Locate every Plasmodium ovale-infected red blood cell.
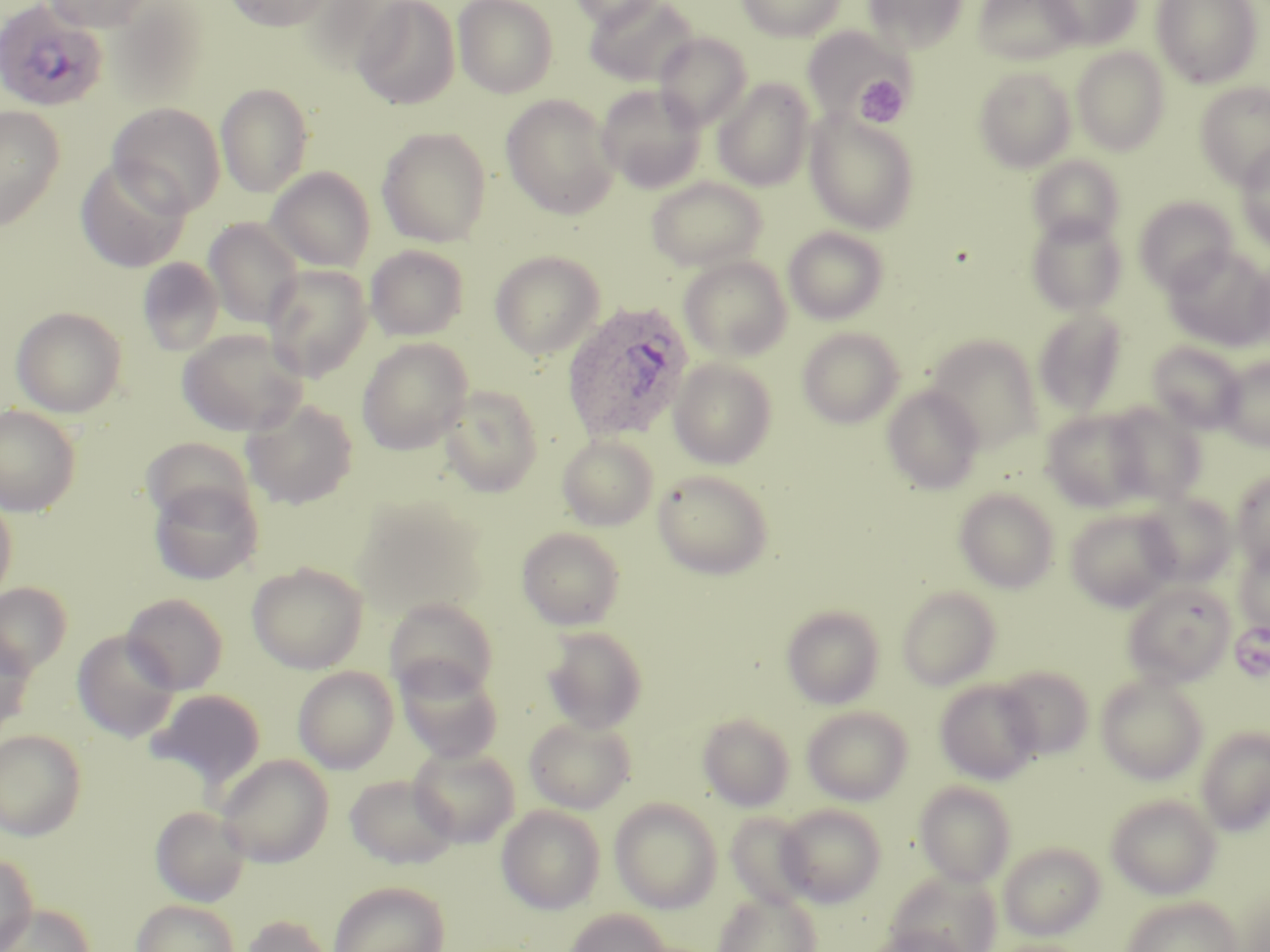
Approximate bounding boxes as (x1,y1)-(x2,y2) corner pairs in pixels.
Plasmodium ovale-infected red blood cells: (0,0)-(109,113), (561,300)-(696,443).

slide-level diagnosis = Plasmodium ovale
uninfected red blood cell locations = approximate bounding boxes as (x1,y1)-(x2,y2) corner pairs in pixels: (40,0)-(159,32), (223,0)-(334,31), (453,0)-(558,98), (568,0)-(671,30), (584,0)-(698,87), (736,0)-(847,40), (863,0)-(968,54), (972,0)-(1082,66), (1039,0)-(1142,50), (1151,0)-(1263,88), (352,1)-(460,109), (802,26)-(913,124), (653,32)-(752,130), (1072,48)-(1170,155), (973,66)-(1076,172), (713,78)-(816,191), (1195,82)-(1270,188), (215,83)-(314,197), (596,84)-(706,192), (501,94)-(620,219), (107,102)-(226,217), (0,106)-(64,233), (805,111)-(921,233), (376,126)-(492,247), (1235,144)-(1270,252), (1027,154)-(1125,246), (74,158)-(191,273), (266,167)-(375,272), (646,176)-(768,272), (1134,197)-(1238,294), (1026,213)-(1127,315), (203,218)-(303,329), (783,226)-(890,325), (365,245)-(468,340), (1163,246)-(1270,351), (489,250)-(605,359), (679,255)-(792,361), (137,257)-(225,357), (1247,263)-(1270,351), (263,264)-(373,381), (11,306)-(127,417), (1032,308)-(1127,418), (797,326)-(905,428), (177,327)-(308,437), (925,334)-(1044,453), (356,338)-(473,455), (1147,341)-(1245,434), (1217,357)-(1270,450), (669,358)-(777,469), (439,384)-(544,497), (882,385)-(984,494), (241,399)-(359,509), (1103,402)-(1206,505), (0,404)-(82,517), (1040,409)-(1153,513), (557,434)-(658,531), (142,437)-(255,527), (653,469)-(774,579), (1231,470)-(1270,571), (149,480)-(263,585), (954,488)-(1060,593), (0,492)-(18,606), (1135,493)-(1237,587), (352,497)-(487,621), (1065,508)-(1180,611), (517,527)-(625,630), (1235,545)-(1270,636), (247,562)-(368,673), (1122,580)-(1236,686), (0,583)-(72,677), (896,586)-(1001,690), (122,593)-(229,694), (384,597)-(498,700), (781,604)-(885,709), (542,627)-(647,733), (0,631)-(36,736), (72,631)-(180,743), (395,657)-(503,762), (996,665)-(1095,759), (293,666)-(399,773), (1096,673)-(1208,785), (935,679)-(1043,784), (147,689)-(265,790), (802,705)-(913,805), (697,713)-(795,811), (524,717)-(636,814), (1196,727)-(1270,835), (0,729)-(86,840), (408,745)-(520,847), (215,753)-(334,867), (344,774)-(458,868), (914,781)-(1016,886), (1105,793)-(1222,899), (610,798)-(722,913), (777,804)-(886,907), (150,805)-(251,906), (496,805)-(606,914), (725,812)-(817,911), (998,841)-(1106,940), (0,853)-(37,951), (886,870)-(1001,952), (328,881)-(451,952), (713,890)-(822,952), (1121,897)-(1243,952), (131,900)-(240,952), (2,903)-(94,952), (563,908)-(672,952), (240,914)-(338,952), (871,925)-(967,952)
platelet locations = approximate bounding boxes as (x1,y1)-(x2,y2) corner pairs in pixels: (855,74)-(909,127)
preparation = thin blood film
magnification = 1000x
stain = May-Grünwald-Giemsa
modality = optical microscopy
field of view = one of a larger specimen
image size = 1270×952 pixels